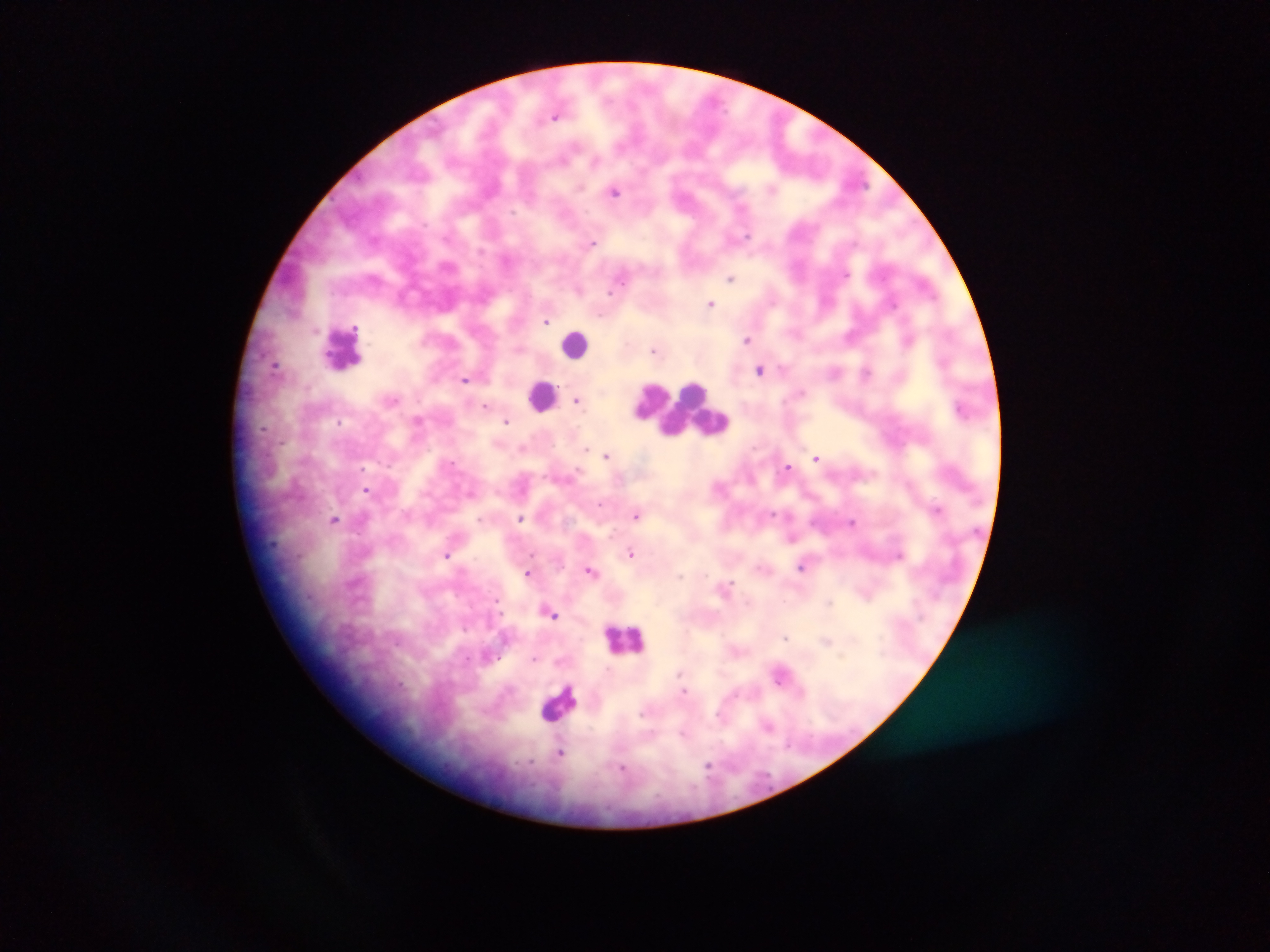

malaria parasite locations = approximate centers as [x, y] in pixels: [556, 114], [615, 191], [593, 242], [731, 278], [712, 303], [546, 321], [747, 338], [909, 338], [656, 350], [277, 364], [759, 370], [867, 372], [466, 378], [578, 400], [486, 405], [417, 420], [507, 421], [339, 422], [607, 455], [816, 456], [787, 467], [367, 490], [601, 504], [938, 509], [637, 514], [520, 518], [335, 520], [853, 522], [790, 537], [631, 553], [447, 554], [803, 566], [591, 570], [530, 572], [726, 586], [550, 611], [785, 637], [827, 639], [535, 658], [782, 674], [768, 725], [561, 752]
field of view = single
leukocyte locations = approximate centers as [x, y] in pixels: [576, 345], [343, 346], [543, 395], [680, 409], [625, 639], [560, 703]
capture = mobile-phone photograph through a microscope
preparation = thick blood smear
image size = 1270×952 pixels
country = Ghana